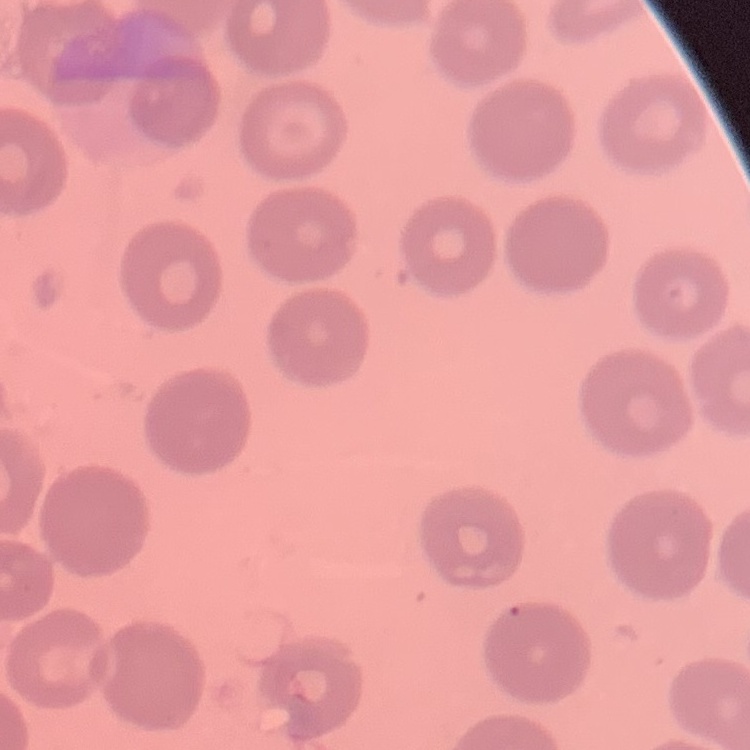

Summary:
  - Red blood cell morphology: no rouleaux formation
  - Stain: Field's or Giemsa
  - Preparation: thin blood smear
  - Image type: square crop of a larger photomicrograph